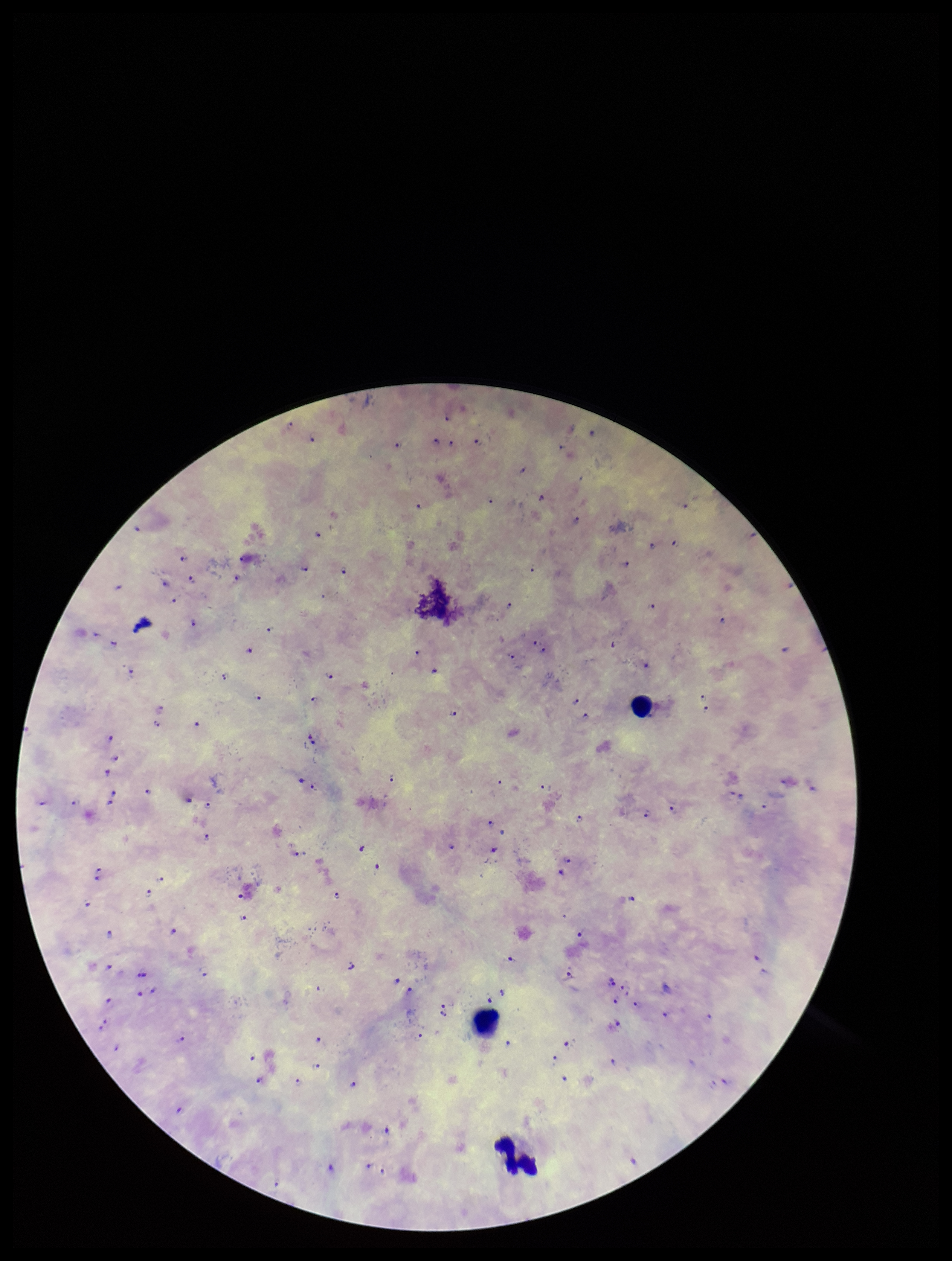

Summary:
  - Image size: 952×1261 pixels
  - Plasmodium parasites: seen
  - Capture: smartphone photograph through the microscope eyepiece
  - Field of view: single
  - Preparation: thick blood smear
  - Species reported for this patient: Plasmodium falciparum
  - Stain: Giemsa
  - Leukocyte count: 3
  - Parasite count: 100
  - Patient malaria status: infected